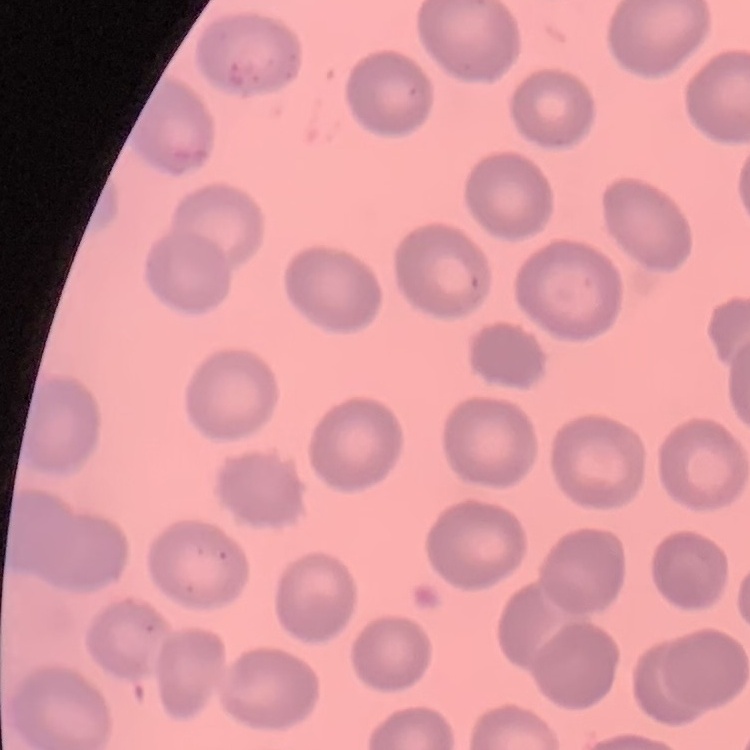
The red blood cells exhibit no rouleaux formation. Stained with either Field's or Giemsa. One tile cut from a larger photomicrograph. Thin blood smear.